Identify the preparation type.
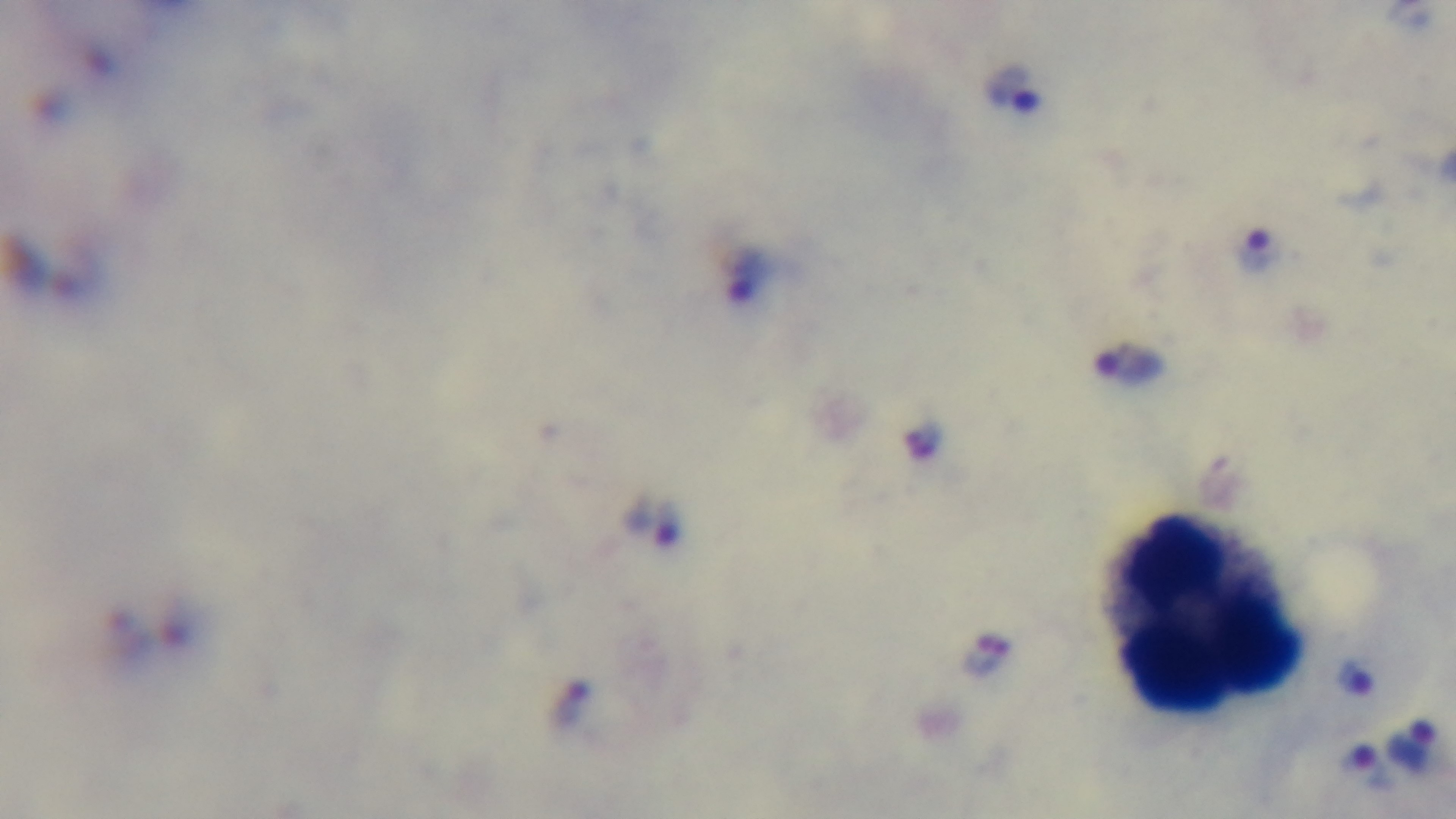

A thick smear.

Oil-immersion objective, 100x. Single field of view. Malaria status: positive. Giemsa-stained. Photomicrograph. Mounted 4K digital camera.